Report the malaria status of this cell.
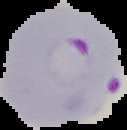

Parasitized.

image type = cell region segmented out of the field of view; surrounding area masked to black
preparation = thin blood film
image size = 127×130 pixels